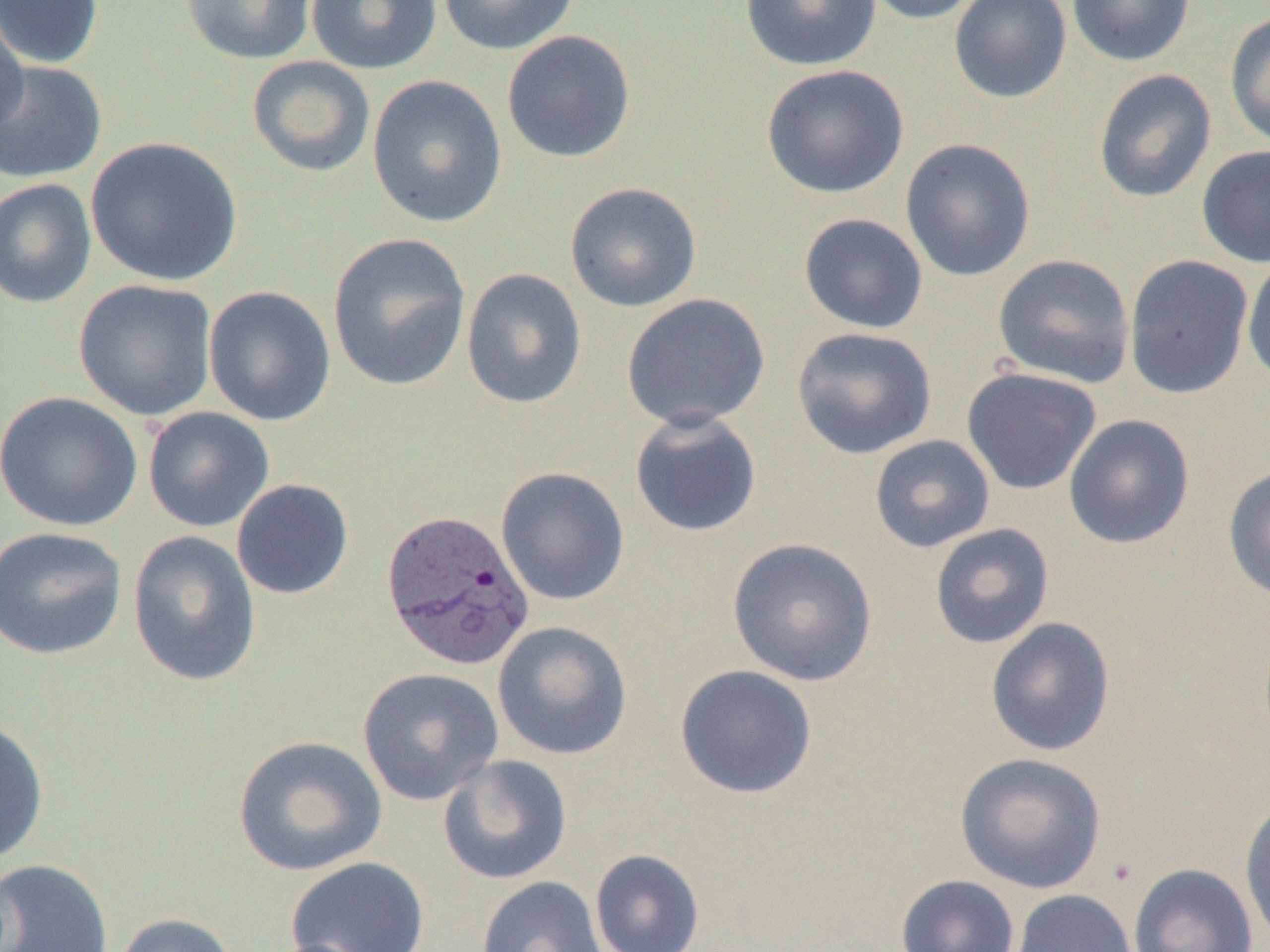 Approximate bounding boxes as (x1,y1)-(x2,y2) corner pairs in pixels. Uninfected red blood cell locations: (0,0)-(104,70), (181,0)-(317,65), (306,0)-(441,75), (436,0)-(580,55), (739,0)-(883,71), (860,0)-(989,25), (948,0)-(1072,104), (1067,0)-(1195,67), (0,8)-(30,143), (1224,11)-(1270,150), (501,30)-(636,163), (247,55)-(376,178), (0,60)-(107,184), (761,64)-(909,199), (1093,69)-(1216,203), (367,75)-(507,228), (86,136)-(242,287), (899,138)-(1036,282), (1196,144)-(1270,268), (0,178)-(97,308), (564,182)-(702,312), (797,213)-(929,334), (327,232)-(472,392), (992,254)-(1136,389), (1123,254)-(1254,400), (1243,254)-(1270,387), (461,268)-(587,409), (73,279)-(218,422), (203,286)-(337,426), (621,293)-(771,430), (791,326)-(937,460), (961,367)-(1102,495), (0,391)-(144,531), (143,406)-(275,533), (629,410)-(762,537), (1063,414)-(1195,549), (869,434)-(995,553), (1222,464)-(1270,604), (495,466)-(630,605), (231,479)-(354,600), (929,523)-(1055,649), (0,526)-(129,660), (127,530)-(261,686), (727,537)-(878,686), (985,617)-(1116,757), (492,620)-(633,760), (674,664)-(818,799), (357,667)-(505,805), (0,719)-(49,864), (233,735)-(388,876), (954,752)-(1107,893), (437,754)-(573,885), (1239,795)-(1270,945), (590,849)-(705,952), (286,856)-(430,952), (0,858)-(114,952), (1127,862)-(1259,952), (896,874)-(1020,952), (476,875)-(607,952), (1011,889)-(1137,952), (111,912)-(239,952). Plasmodium vivax-infected red blood cell locations: (380,508)-(536,672). Slide-level diagnosis: Plasmodium vivax. Thin blood smear. One field of a larger specimen. Image is 1270×952 pixels. Light microscopy. 1000x magnification.